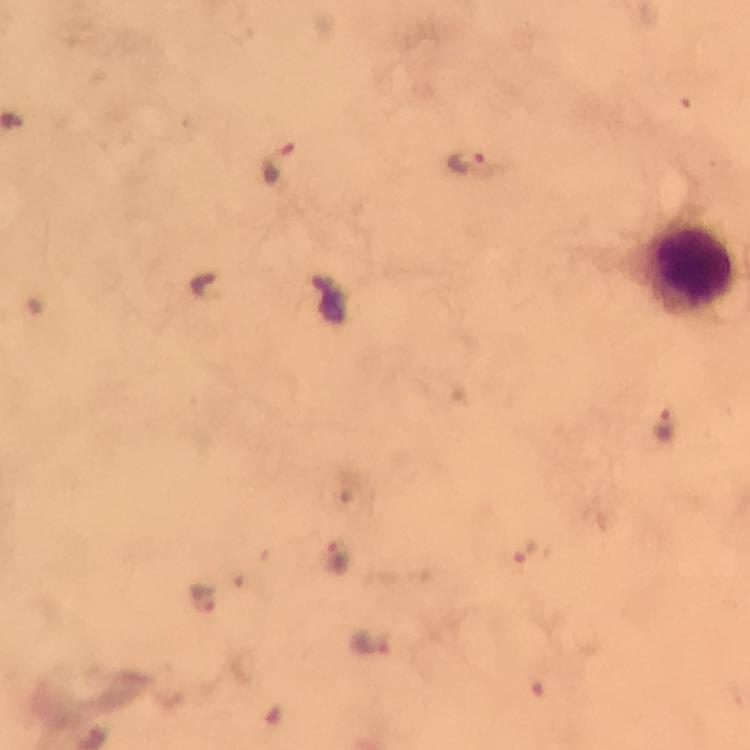

capture = smartphone mounted on the microscope
malaria parasite locations = approximate centers as [x, y] in pixels: [277, 163], [469, 166], [202, 287], [662, 423], [337, 555], [204, 598], [366, 639]
preparation = thick blood smear
leukocyte locations = approximate centers as [x, y] in pixels: [692, 265]
image size = 750×750 pixels
immersion oil = used
magnification = 100x
stain = Giemsa
cropped from = one field of view
context = from a diagnostic examination for malaria